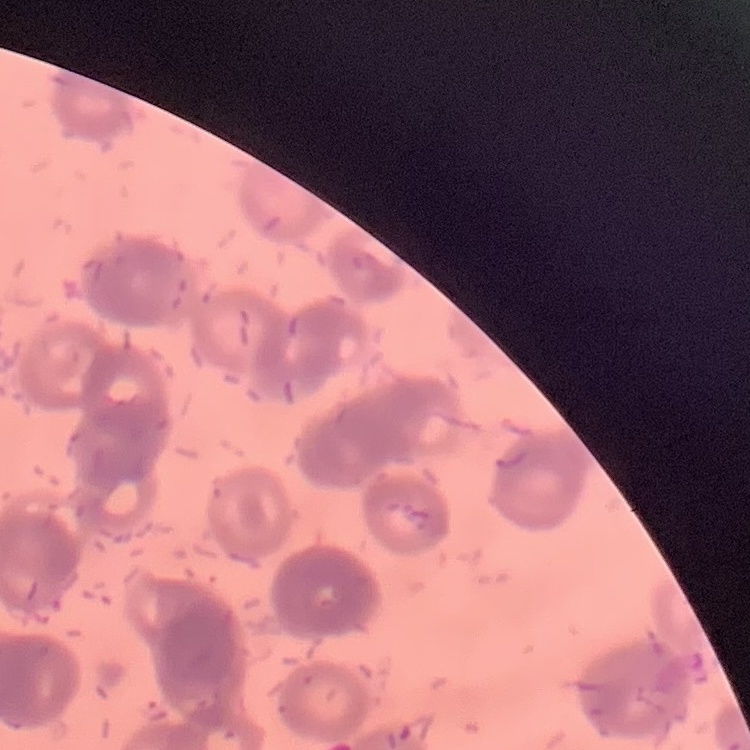
The erythrocytes exhibit rouleaux formation. Square crop of a larger photomicrograph. Field's or Giemsa stain. Thin blood film.